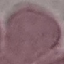

Summary:
  - Result: negative for malaria parasites
  - Image type: cell patch, automatically extracted from a larger field of view and resized to 64 × 64 pixels
  - Capture: smartphone through the microscope eyepiece
  - Preparation: thin smear
  - Stain: Giemsa